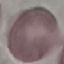

Summary:
  - Result: negative for malaria parasites
  - Image type: cell patch, automatically extracted from a larger field of view and resized to 64 × 64 pixels
  - Stain: Giemsa
  - Capture: smartphone through the microscope eyepiece
  - Preparation: thin blood film